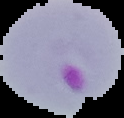

Summary:
  - Result: malaria parasites identified
  - Preparation: thin blood film
  - Image type: segmented cell region with the area outside set to black
  - Image size: 124×118 pixels